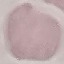

Result: no malaria parasites seen. Giemsa stain. Photographed with a smartphone camera at the microscope eyepiece. Thin blood smear. Automatically extracted cell patch, resized to 64 × 64 pixels.